Draw a bounding box around every Plasmodium parasite.
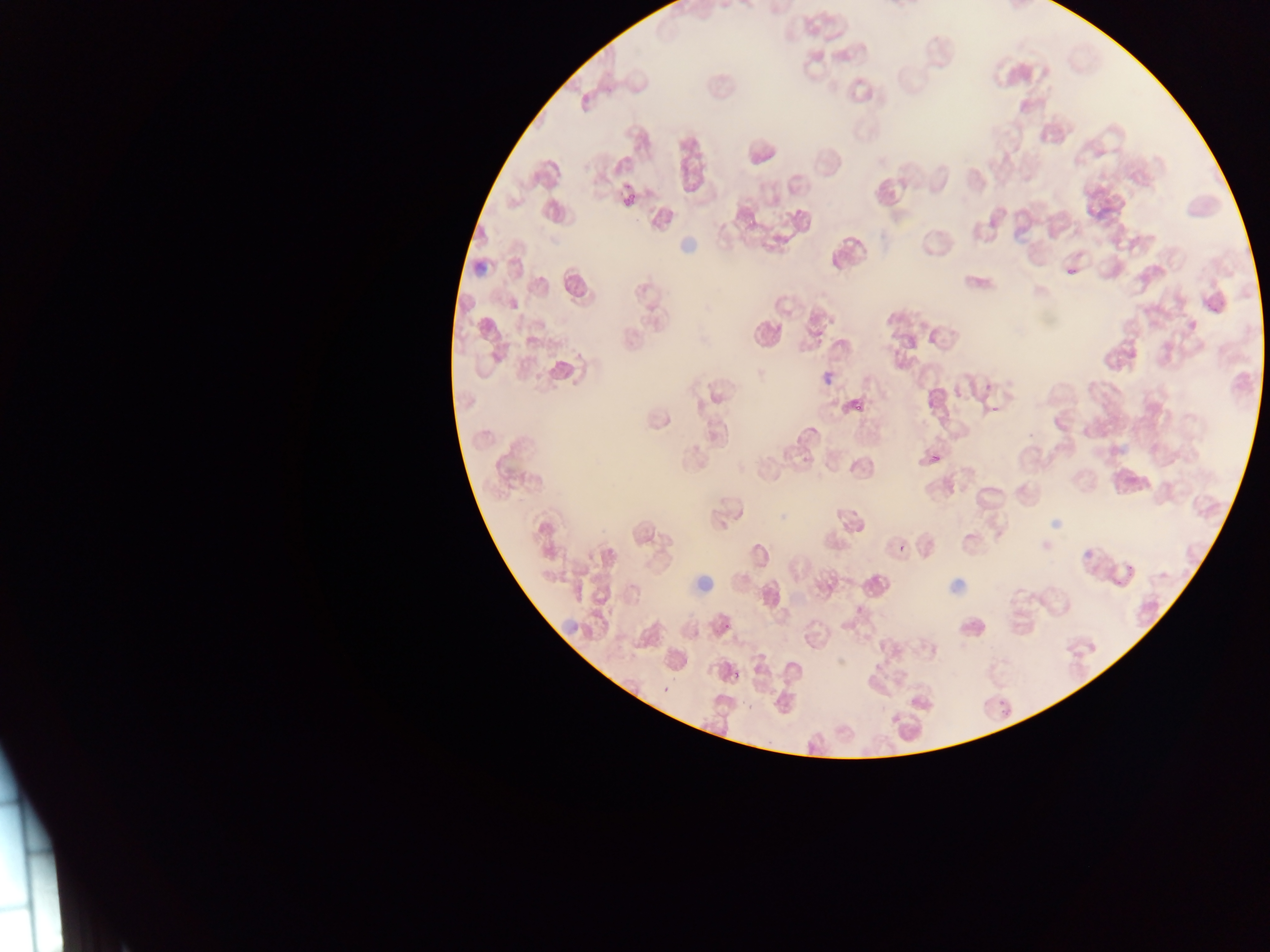

Approximate bounding boxes as [left, top, right, bottom] in pixels.
Plasmodium parasites: [621, 189, 640, 210], [1064, 263, 1078, 278], [822, 371, 838, 386], [845, 394, 868, 417], [985, 406, 1002, 413], [925, 447, 945, 464], [891, 534, 908, 553], [718, 622, 731, 628], [732, 670, 740, 681], [659, 688, 670, 694], [998, 698, 1006, 707].

image size = 1270×952 pixels
country = Ghana
field of view = single
preparation = thin blood smear
capture = mobile-phone photograph through a microscope